Locate every blood parasite and identify its species.
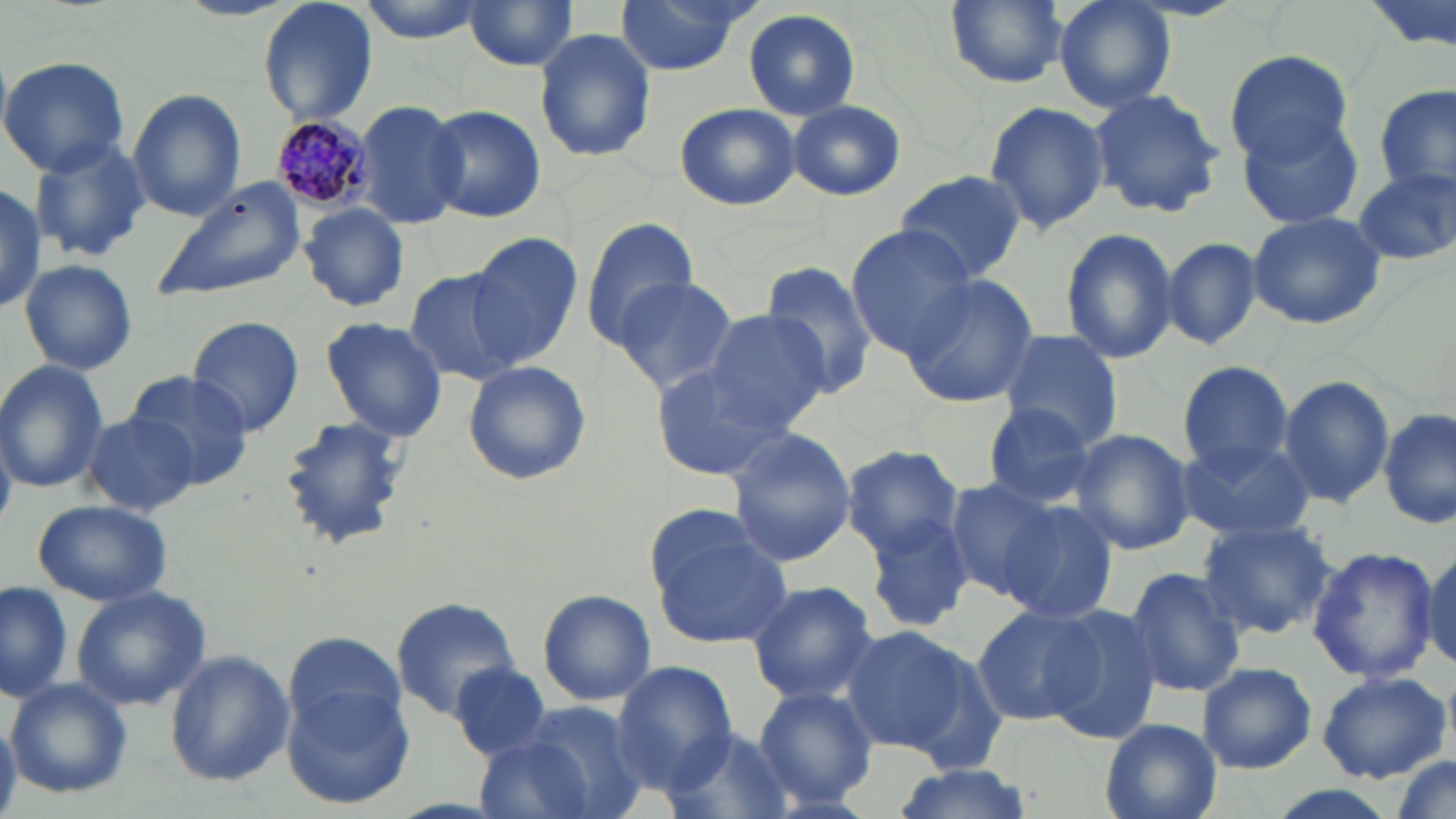
Approximate bounding boxes as [x1, y1, x2, y2] in pixels.
Plasmodium malariae-infected red blood cells: [269, 115, 374, 214].
No Plasmodium falciparum, Plasmodium ovale, Plasmodium vivax, Babesia divergens, or Trypanosoma brucei observed.

Uninfected red blood cell locations: [258, 0, 377, 129], [352, 0, 493, 41], [464, 0, 580, 72], [611, 0, 750, 74], [945, 0, 1067, 87], [1055, 0, 1175, 113], [742, 8, 861, 121], [533, 26, 657, 163], [1226, 49, 1357, 164], [0, 56, 131, 176], [1375, 84, 1455, 197], [127, 89, 246, 221], [1090, 89, 1225, 217], [787, 99, 905, 201], [983, 99, 1109, 235], [354, 100, 467, 230], [673, 102, 800, 211], [425, 104, 547, 223], [1239, 111, 1367, 230], [27, 140, 153, 263], [1353, 167, 1455, 266], [893, 171, 1027, 282], [150, 177, 309, 304], [1, 184, 45, 311], [300, 204, 409, 311], [1247, 210, 1389, 330], [581, 218, 700, 345], [845, 227, 978, 360], [1059, 227, 1179, 364], [466, 232, 582, 367], [1162, 236, 1264, 351], [19, 259, 138, 375], [761, 259, 880, 401], [403, 268, 522, 385], [899, 272, 1039, 409], [608, 275, 737, 395], [702, 307, 836, 430], [187, 315, 305, 436], [320, 317, 447, 442], [996, 330, 1126, 449], [0, 361, 107, 493], [462, 361, 591, 486], [1176, 361, 1297, 475], [650, 362, 798, 482], [123, 369, 256, 489], [1278, 375, 1394, 508], [980, 402, 1102, 510], [1380, 407, 1455, 532], [81, 411, 197, 516], [278, 413, 409, 550], [727, 428, 856, 566], [1068, 428, 1196, 555], [1175, 438, 1315, 544], [840, 444, 967, 562], [941, 479, 1062, 602], [29, 499, 173, 606], [999, 502, 1120, 623], [860, 511, 975, 634], [1197, 518, 1338, 640], [649, 519, 795, 650], [1420, 544, 1456, 674], [1307, 546, 1439, 685], [1125, 566, 1246, 697], [0, 578, 72, 705], [744, 580, 880, 705], [71, 585, 210, 711], [537, 589, 655, 706], [391, 597, 521, 719], [1043, 604, 1163, 745], [971, 605, 1100, 726], [834, 625, 975, 756], [284, 629, 405, 746], [164, 649, 293, 787], [612, 661, 735, 792], [1197, 661, 1317, 774], [447, 665, 552, 758], [1316, 670, 1451, 783], [6, 678, 132, 799], [283, 685, 415, 811], [752, 686, 879, 810], [479, 700, 651, 819], [0, 719, 20, 817], [1098, 719, 1222, 819], [661, 726, 787, 819], [1387, 756, 1453, 818], [887, 764, 1037, 819]. Slide-level diagnosis: Plasmodium malariae. Optical microscopy. May-Grünwald-Giemsa-stained preparation. Single field of view. 1000x magnification. Image is 1456×819 pixels. Thin blood smear.